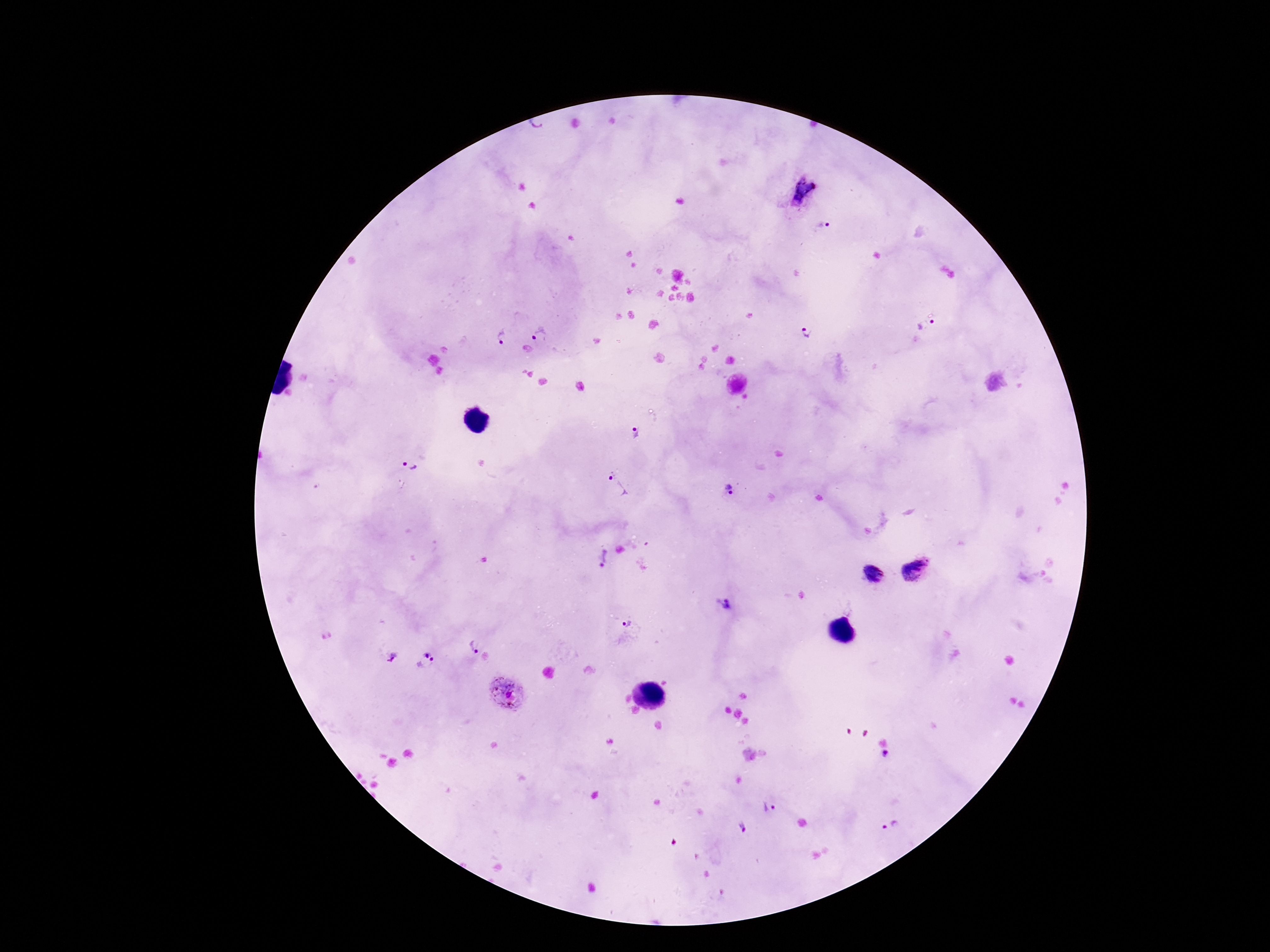

Approximate centers as {x, y} in pixels.
Summary:
  - Plasmodium parasite locations: {537, 126}, {821, 225}, {927, 326}, {807, 333}, {542, 334}, {501, 337}, {637, 434}, {407, 467}, {618, 485}, {729, 490}, {603, 557}, {914, 570}, {872, 574}, {726, 604}, {626, 624}, {472, 644}, {394, 659}, {426, 662}, {506, 691}, {885, 754}, {768, 808}, {892, 827}, {742, 828}
  - Capture: smartphone camera through the microscope eyepiece
  - Image size: 1270×952 pixels
  - Stain: Giemsa
  - Magnification: 100x
  - Patient malaria status: positive
  - Preparation: thick peripheral-blood smear
  - Field of view: single